Classify this cell by malaria status.
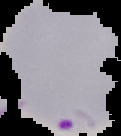
It is parasitized.

Summary:
  - Preparation: thin blood film
  - Image size: 121×136 pixels
  - Image type: segmented cell region with the area outside set to black